Classify this cell by malaria status.
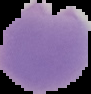
It is parasitized.

Summary:
  - Image size: 91×94 pixels
  - Preparation: thin blood film
  - Image type: cell region segmented out of the field of view; surrounding area masked to black